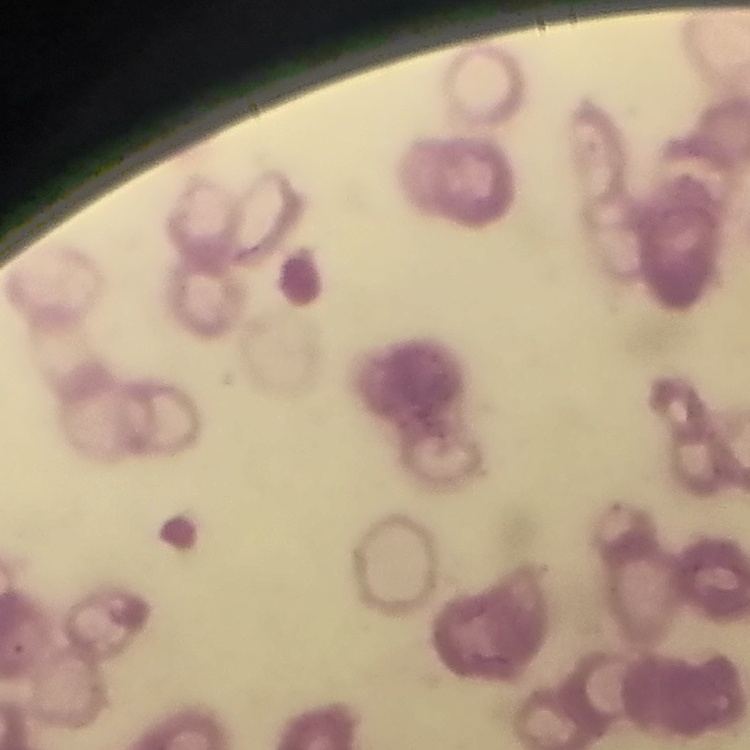 The red blood cells show rouleaux formation. Stained with either Field's or Giemsa. Thin blood smear. One tile cut from a larger photomicrograph.